Name the cell type shown.
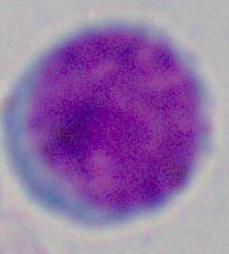

A leukocyte.

1000x magnification. Micrograph.